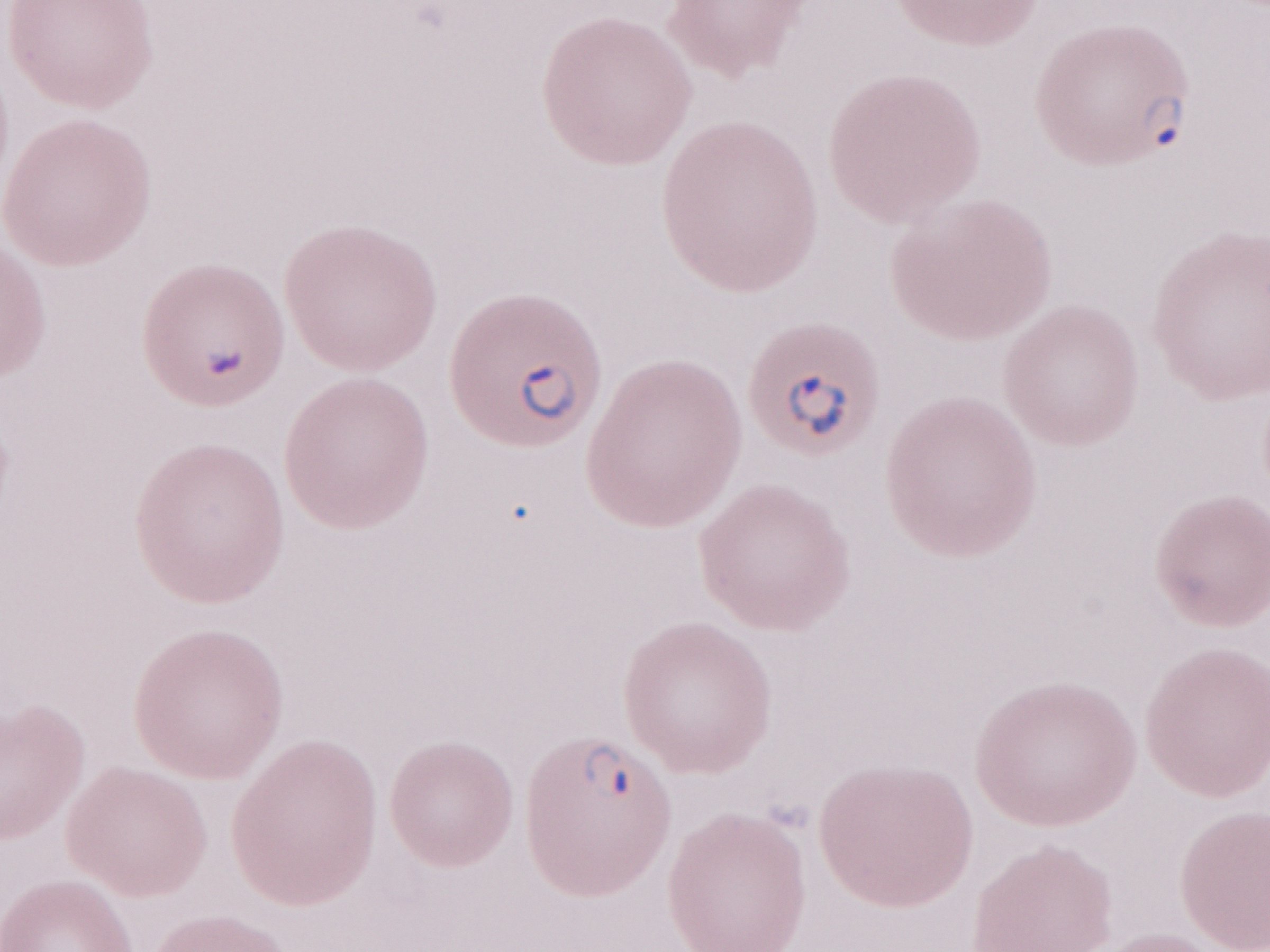

Single field of view. 1,000x magnification. Olympus BX43 microscope and DP73 digital camera. Patient diagnosis: malaria infection. Thin blood film. May-Grünwald-Giemsa stain. Image is 1270×952 pixels.